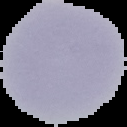 The area outside the segmented cell region is set to black. From a thin blood film. Result: negative for malaria parasites. Image is 127×127 pixels.